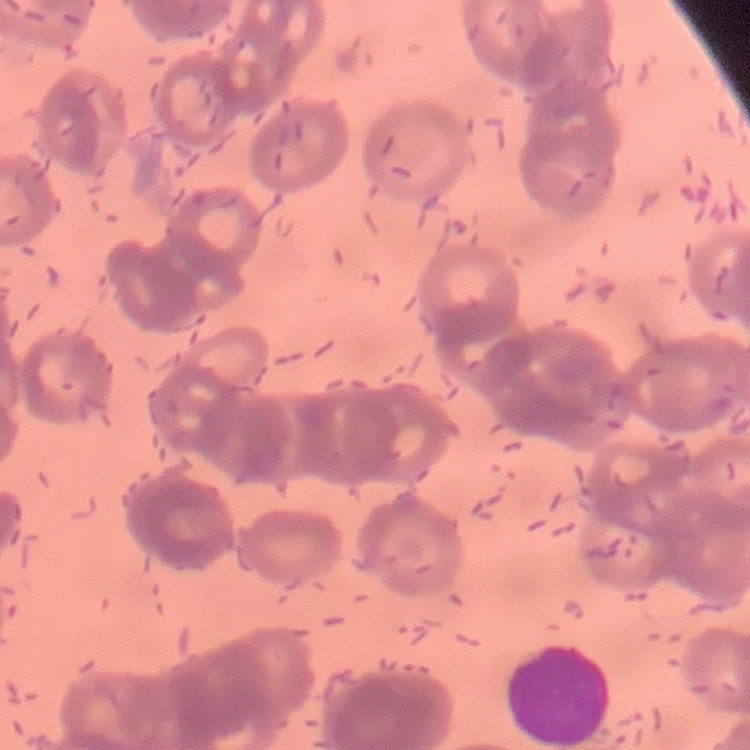
The red blood cells show rouleaux formation. Square crop of a larger photomicrograph. Thin blood smear. Field's or Giemsa stain.